Name the parasite shown.
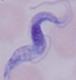
A trypanosome.

Micrograph. Captured at 1000x magnification.